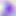
magnification = 400x
identification = Toxoplasma gondii
modality = micrograph